State which parasite is depicted.
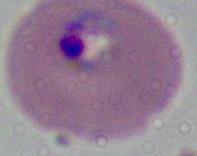
This is Plasmodium.

400x or 1000x magnification. Micrograph.